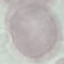 Malaria status: uninfected. Cell patch, automatically extracted from a larger field of view and resized to 64 × 64 pixels. Thin blood smear. Giemsa-stained preparation. Acquired by smartphone through the microscope eyepiece.